Assess this cell for malaria.
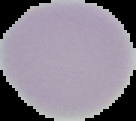

Uninfected.

{
  "preparation": "thin blood smear",
  "image_type": "segmented cell region with the area outside set to black",
  "image_size": "136×121 pixels"
}